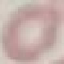

Result: negative for malaria parasites. Giemsa-stained preparation. Photographed with a smartphone camera at the microscope eyepiece. Thin blood film. Cell patch, automatically extracted from a larger field of view and resized to 64 × 64 pixels.